Report the malaria status of this cell.
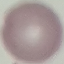
It is uninfected.

Acquired by smartphone through the microscope eyepiece. Automatically extracted cell patch, resized to 64 × 64 pixels. Giemsa-stained preparation. Thin blood smear.